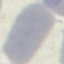
Result: no malaria parasites detected. Cell patch, automatically extracted from a larger field of view and resized to 64 × 64 pixels. Thin blood film. Acquired by smartphone through the microscope eyepiece. Giemsa-stained preparation.